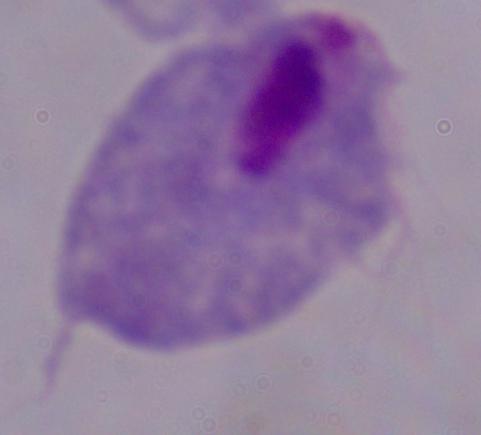
identification = trichomonad
modality = photomicrograph
magnification = 1000x